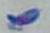

Summary:
  - Identification: Toxoplasma gondii
  - Modality: micrograph
  - Magnification: 1000x